Give the position of every leukocyte visible.
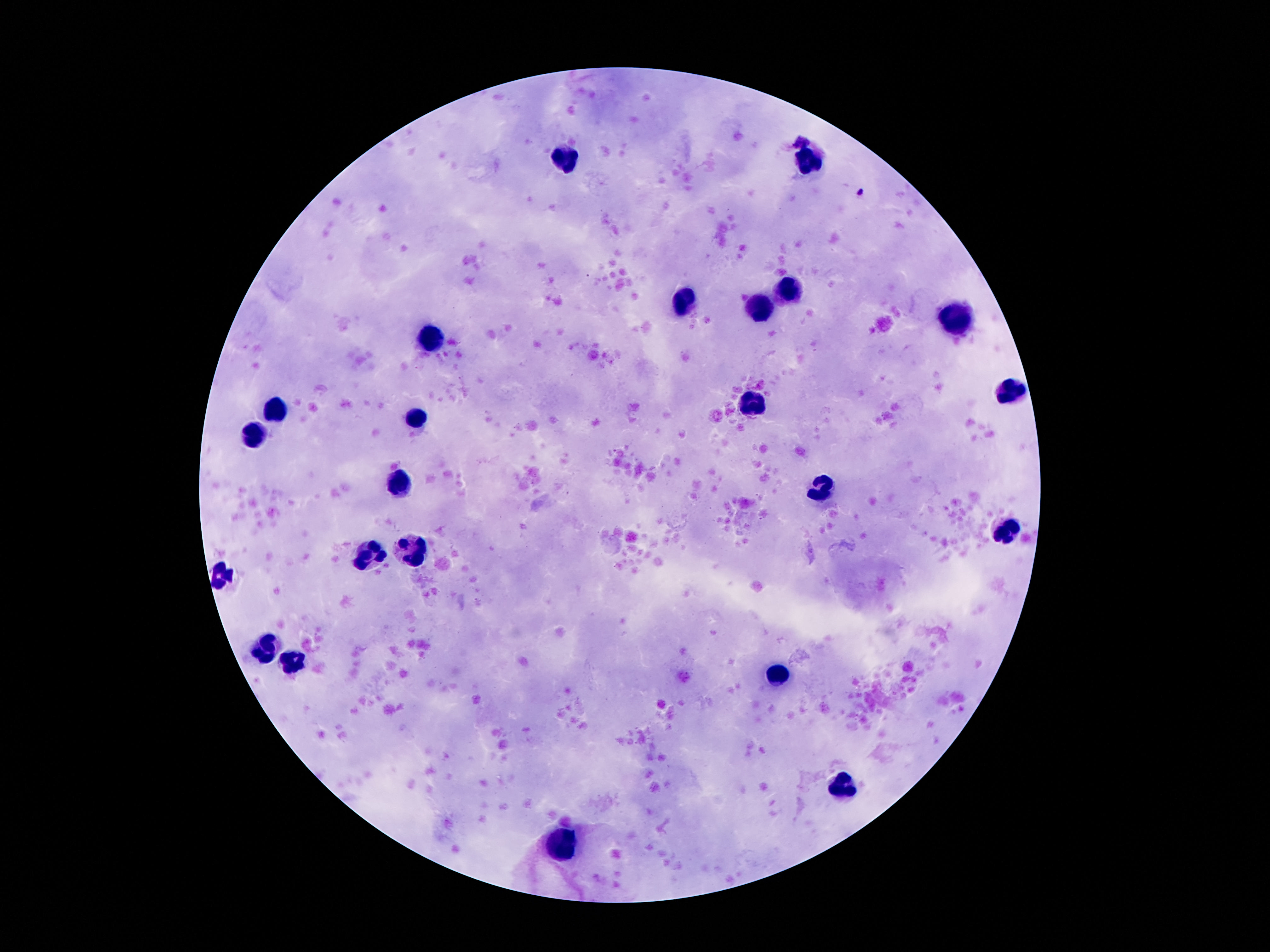

Approximate centers as {x, y} in pixels.
Leukocytes: {565, 156}, {809, 160}, {788, 288}, {687, 299}, {760, 307}, {956, 319}, {433, 332}, {1010, 389}, {752, 403}, {275, 409}, {418, 418}, {254, 433}, {401, 484}, {819, 490}, {1004, 531}, {414, 549}, {370, 553}, {223, 576}, {260, 648}, {294, 663}, {777, 674}, {844, 785}, {561, 843}.

Giemsa stain. Image is 1270×952 pixels. Thick peripheral-blood smear. One field from this slide. Patient malaria status: uninfected. Photographed through the microscope eyepiece with a smartphone camera. 100x magnification.